State which parasite is depicted.
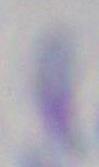
This is Toxoplasma gondii.

magnification = 1000x
modality = micrograph